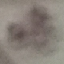
result = no malaria parasites seen
capture = smartphone through the microscope eyepiece
image type = cell patch, automatically extracted from a larger field of view and resized to 64 × 64 pixels
preparation = thin blood smear
stain = Giemsa